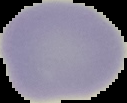
preparation = thin blood smear
image type = cell region segmented out of the field of view; surrounding area masked to black
result = negative for Plasmodium parasites
image size = 127×103 pixels